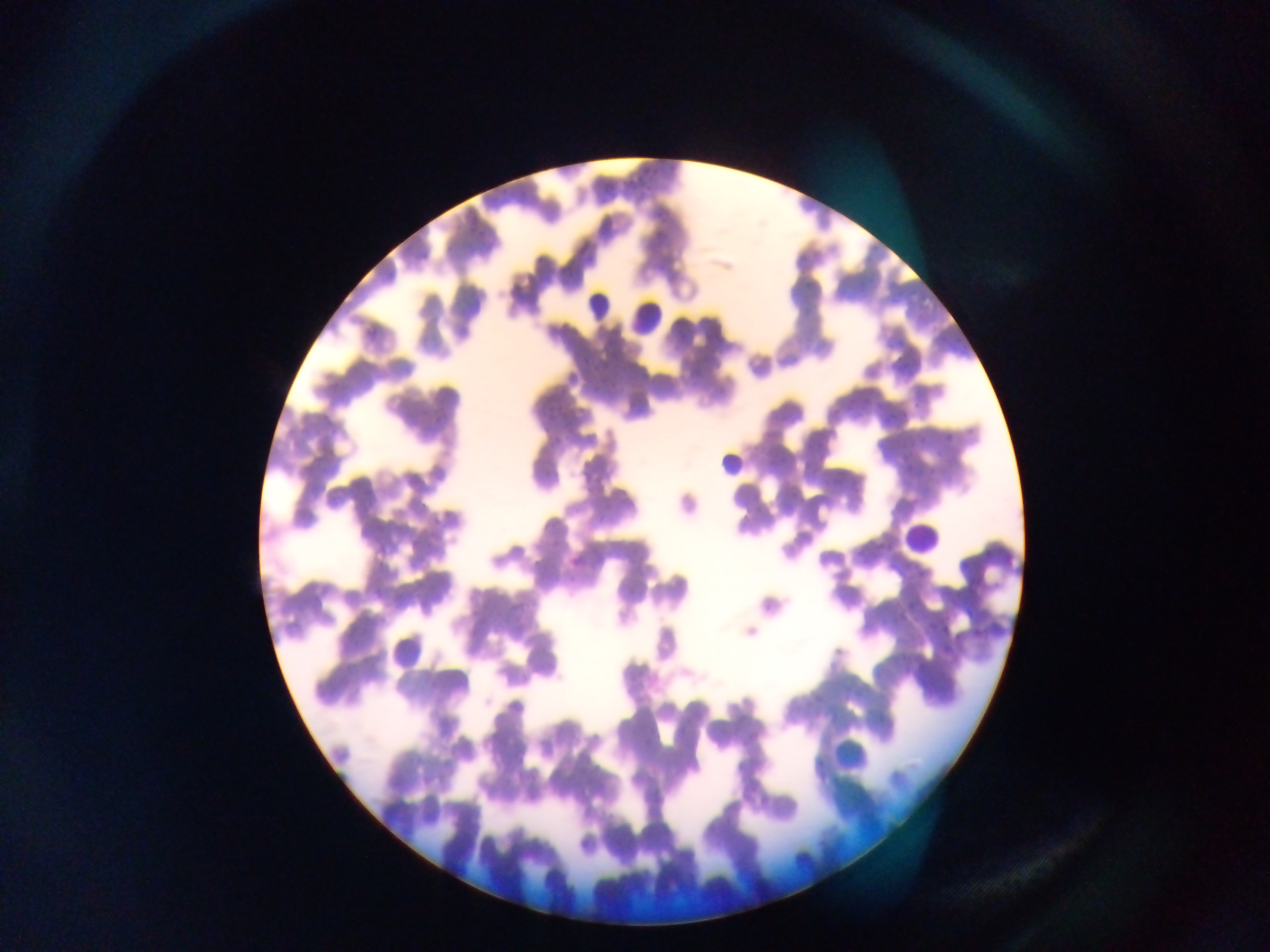

Approximate bounding boxes as {left, top, right, bottom} in pixels. Malaria parasite locations: {803, 278, 815, 293}, {581, 356, 591, 364}, {589, 365, 602, 373}, {600, 378, 609, 386}, {546, 407, 558, 419}, {884, 410, 899, 426}, {945, 432, 954, 440}, {554, 434, 562, 442}, {900, 446, 913, 460}, {914, 470, 924, 480}. Leukocyte locations: {578, 293, 621, 334}, {630, 301, 663, 342}, {709, 449, 747, 480}, {904, 513, 942, 554}, {395, 626, 429, 674}, {834, 733, 878, 771}. One field of view. Mobile-phone photograph taken through the microscope. Image is 1270×952 pixels. Sample from Ghana. Thin blood film.